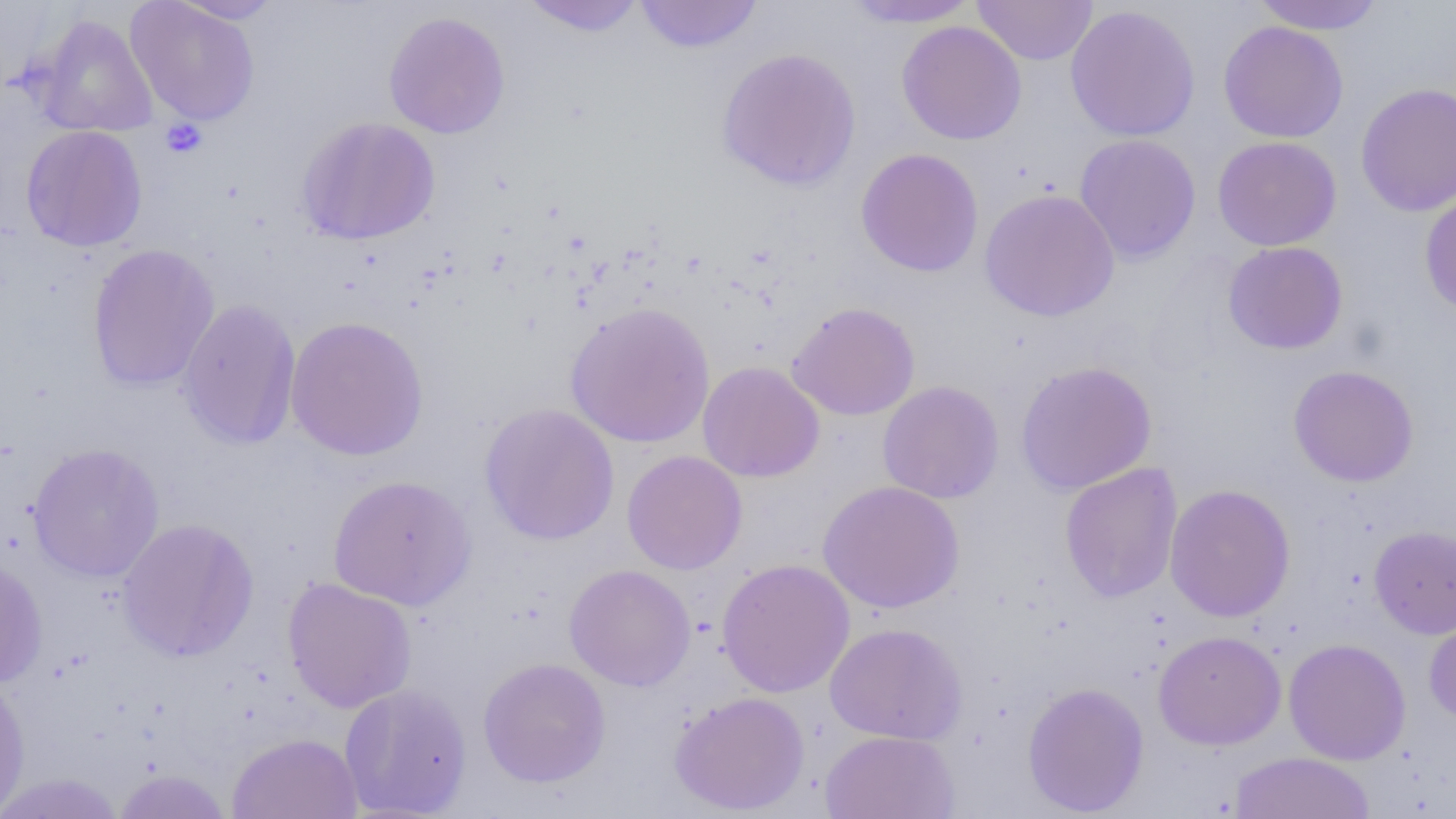

Approximate bounding boxes as [x1, y1, x2, y2] in pixels. Uninfected red blood cell locations: [168, 0, 284, 24], [519, 0, 647, 37], [633, 0, 764, 54], [839, 0, 982, 28], [972, 0, 1097, 65], [1251, 0, 1386, 34], [125, 1, 261, 127], [1064, 5, 1201, 142], [383, 11, 511, 139], [30, 14, 158, 138], [897, 20, 1027, 145], [1218, 21, 1348, 143], [716, 47, 861, 191], [1355, 82, 1456, 216], [296, 116, 440, 246], [21, 125, 147, 252], [1074, 134, 1201, 263], [1212, 136, 1342, 251], [855, 148, 984, 277], [979, 188, 1119, 322], [1419, 189, 1456, 316], [1223, 241, 1348, 355], [87, 243, 220, 392], [178, 299, 301, 450], [565, 302, 715, 448], [786, 302, 920, 421], [285, 316, 430, 461], [697, 361, 825, 483], [1014, 361, 1158, 495], [1288, 365, 1420, 487], [878, 381, 1004, 504], [479, 403, 619, 545], [27, 443, 165, 582], [622, 450, 748, 575], [1059, 462, 1183, 603], [328, 474, 476, 610], [818, 480, 965, 614], [1164, 483, 1296, 623], [116, 518, 259, 662], [1369, 524, 1456, 638], [0, 555, 48, 689], [716, 558, 855, 698], [564, 564, 696, 691], [282, 577, 417, 713], [1423, 612, 1456, 725], [825, 622, 968, 746], [1153, 630, 1286, 750], [1283, 637, 1411, 764], [478, 657, 611, 788], [0, 673, 31, 818], [1022, 681, 1149, 817], [339, 682, 472, 818], [669, 691, 810, 815], [821, 730, 960, 819], [227, 732, 362, 819], [1230, 752, 1376, 818], [111, 769, 233, 818], [0, 773, 125, 818]. Platelet locations: [160, 118, 208, 159]. Slide-level diagnosis: no evidence of blood parasites. Optical microscopy. Captured at 1000x magnification. Single field of view. Image is 1456×819 pixels. Thin blood film.